Name the parasite shown.
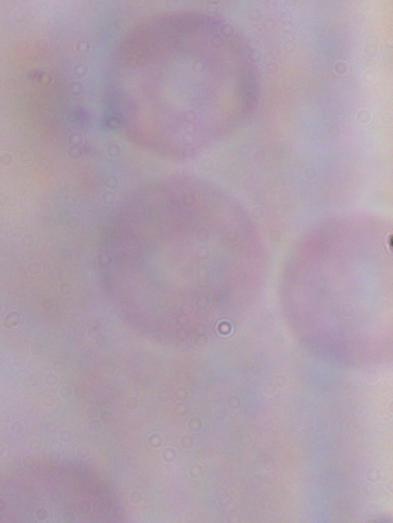

This is a trypanosome.

1000x magnification. Photomicrograph.